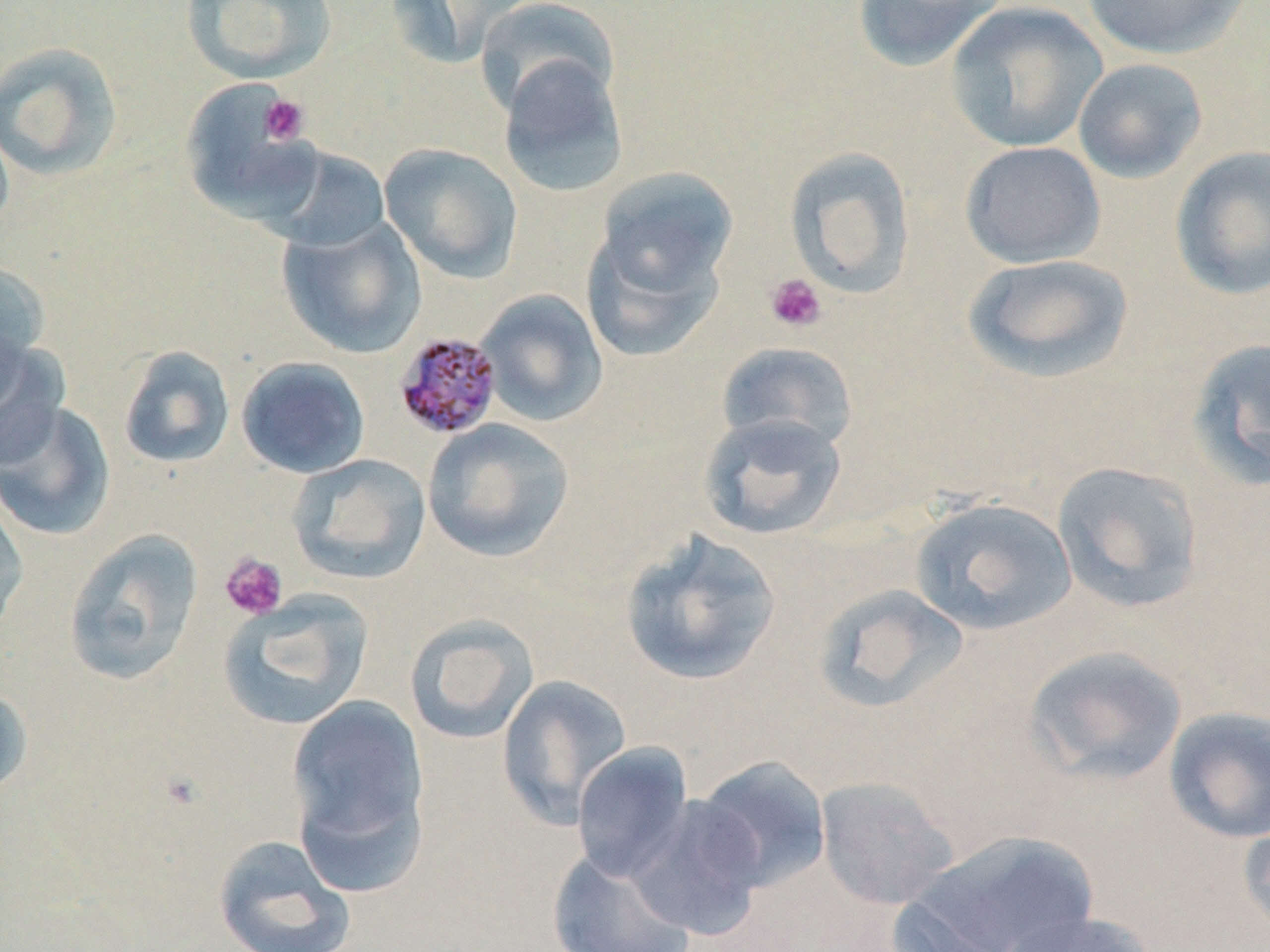
Summary:
  - Coordinate format: approximate bounding boxes as [x1, y1, x2, y2] in pixels
  - Uninfected red blood cell locations: [180, 0, 338, 83], [385, 0, 531, 69], [474, 0, 620, 119], [850, 0, 1009, 71], [1079, 0, 1252, 60], [944, 1, 1108, 153], [0, 41, 124, 182], [497, 54, 629, 199], [1073, 57, 1208, 184], [179, 79, 321, 225], [0, 119, 14, 239], [959, 141, 1106, 268], [258, 143, 392, 252], [379, 143, 523, 283], [784, 146, 917, 298], [1169, 146, 1270, 301], [595, 168, 738, 300], [277, 217, 426, 359], [581, 224, 727, 364], [962, 253, 1135, 383], [0, 258, 50, 394], [476, 289, 608, 427], [1186, 337, 1270, 492], [0, 338, 67, 467], [716, 341, 859, 454], [118, 345, 236, 469], [236, 357, 370, 479], [0, 400, 116, 541], [697, 413, 848, 541], [422, 418, 575, 563], [287, 454, 431, 584], [1051, 460, 1205, 613], [0, 488, 30, 638], [909, 496, 1078, 635], [63, 528, 204, 686], [618, 530, 783, 686], [811, 582, 970, 714], [217, 590, 373, 731], [404, 614, 539, 745], [1023, 645, 1188, 786], [495, 674, 632, 829], [0, 684, 33, 800], [286, 693, 430, 885], [1162, 707, 1270, 844], [570, 742, 694, 883], [693, 755, 831, 892], [815, 776, 960, 910], [629, 794, 768, 938], [1237, 810, 1270, 938], [911, 831, 1097, 952], [212, 834, 357, 952], [546, 849, 697, 952], [887, 896, 1024, 952], [997, 909, 1160, 952]
  - Platelet locations: [260, 94, 310, 146], [764, 273, 827, 333], [219, 552, 288, 620]
  - Plasmodium malariae-infected red blood cell locations: [393, 330, 503, 440]
  - Slide-level diagnosis: Plasmodium malariae
  - Preparation: thin blood film
  - Field of view: one of a larger specimen
  - Image size: 1270×952 pixels
  - Modality: optical microscopy
  - Magnification: 1000x
  - Stain: May-Grünwald-Giemsa